Report the malaria status of this cell.
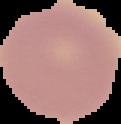

Uninfected.

Segmented cell region on a black background. Image is 121×124 pixels. From a thin blood smear.